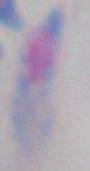

Summary:
  - Modality: photomicrograph
  - Magnification: 1000x
  - Identification: Toxoplasma gondii